Locate and identify every blood parasite.
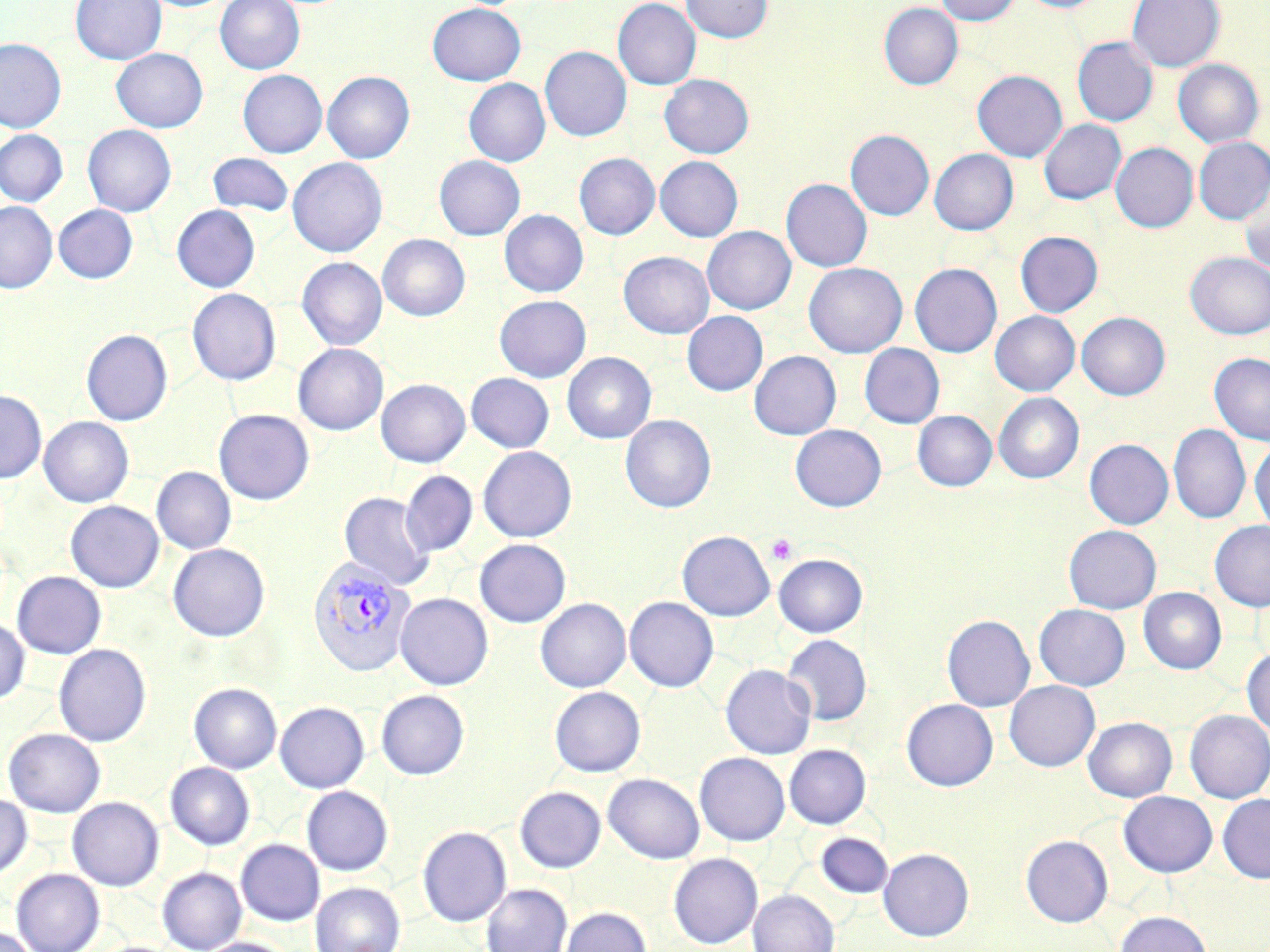

Approximate bounding boxes as (x1, y1, x2, y2) in pixels.
Plasmodium vivax-infected red blood cells: (308, 557, 417, 676).
No Plasmodium falciparum, Plasmodium ovale, Plasmodium malariae, Babesia divergens, or Trypanosoma brucei observed.

Summary:
  - Platelet locations: (767, 534, 798, 565)
  - Uninfected red blood cell locations: (70, 0, 166, 64), (215, 0, 304, 74), (613, 0, 701, 89), (681, 0, 773, 42), (935, 0, 1020, 25), (1017, 0, 1107, 13), (1127, 0, 1225, 72), (426, 3, 526, 85), (878, 3, 963, 90), (1072, 37, 1158, 126), (0, 38, 66, 132), (540, 45, 631, 141), (111, 48, 208, 133), (1173, 59, 1263, 147), (237, 70, 327, 157), (972, 70, 1067, 161), (322, 71, 415, 163), (660, 74, 754, 159), (464, 78, 550, 166), (1039, 119, 1126, 205), (82, 124, 176, 216), (0, 130, 68, 206), (845, 130, 934, 220), (1194, 137, 1270, 224), (1111, 142, 1198, 232), (929, 149, 1018, 235), (208, 152, 293, 217), (574, 153, 659, 239), (434, 155, 526, 240), (655, 156, 743, 242), (287, 157, 387, 257), (781, 179, 872, 272), (1239, 188, 1270, 274), (0, 201, 57, 292), (53, 204, 138, 283), (172, 205, 259, 292), (499, 210, 588, 297), (702, 226, 796, 314), (1015, 231, 1103, 317), (378, 234, 470, 321), (618, 252, 714, 338), (1185, 252, 1270, 339), (297, 257, 387, 350), (803, 262, 907, 357), (910, 263, 1002, 357), (187, 288, 281, 386), (494, 295, 591, 382), (682, 311, 768, 396), (990, 311, 1079, 395), (1077, 312, 1170, 400), (81, 329, 173, 426), (293, 343, 388, 435), (859, 343, 944, 429), (749, 350, 841, 440), (562, 352, 656, 443), (1210, 352, 1270, 445), (466, 373, 554, 452), (376, 379, 470, 467), (0, 390, 46, 482), (993, 392, 1084, 483), (214, 409, 314, 505), (912, 410, 997, 491), (620, 414, 716, 512), (39, 417, 134, 507), (790, 424, 886, 511), (1169, 425, 1250, 523), (1085, 439, 1173, 529), (1250, 442, 1270, 535), (478, 446, 577, 543), (152, 466, 236, 555), (401, 471, 478, 556), (339, 492, 435, 591), (66, 500, 164, 591), (1210, 520, 1270, 611), (1063, 525, 1161, 614), (677, 530, 775, 621), (474, 539, 570, 627), (168, 544, 269, 641), (774, 553, 867, 637), (12, 571, 106, 659), (1139, 587, 1226, 674), (395, 593, 493, 690), (624, 597, 718, 692), (535, 598, 631, 692), (1034, 604, 1130, 690), (942, 614, 1035, 711), (0, 618, 30, 704), (783, 634, 872, 726), (53, 643, 151, 746), (1242, 648, 1270, 735), (720, 664, 816, 759), (1004, 680, 1100, 771), (189, 682, 282, 773), (549, 686, 645, 776), (376, 690, 469, 780), (902, 699, 998, 790), (275, 702, 369, 793), (1185, 710, 1270, 802), (1083, 717, 1177, 802), (4, 728, 105, 817), (784, 744, 871, 828), (694, 752, 790, 845), (165, 762, 255, 850), (603, 773, 704, 863), (301, 786, 393, 875), (515, 786, 605, 872), (1119, 791, 1218, 876), (1218, 793, 1270, 883), (0, 794, 32, 879), (68, 797, 163, 890), (418, 826, 511, 926), (815, 833, 894, 899), (1021, 835, 1113, 927), (236, 839, 324, 925), (878, 848, 974, 941), (669, 853, 762, 948), (157, 867, 247, 951), (11, 868, 105, 952), (311, 881, 405, 952), (481, 883, 572, 952), (748, 890, 839, 952), (560, 906, 652, 952), (1115, 911, 1212, 952), (0, 925, 40, 952), (197, 937, 297, 952)
  - Slide-level diagnosis: Plasmodium vivax
  - Stain: May-Grünwald-Giemsa
  - Field of view: one of a larger specimen
  - Magnification: 1000x
  - Modality: light microscopy
  - Preparation: thin blood smear
  - Image size: 1270×952 pixels